Classify this cell by malaria status.
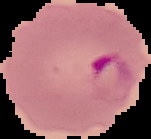

Parasitized.

The area outside the segmented cell region is set to black. From a thin blood film. Image is 151×139 pixels.